Identify the parasite.
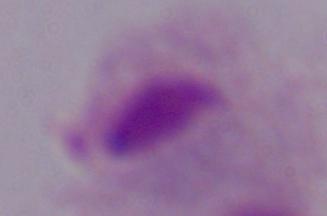
A trichomonad.

Summary:
  - Magnification: 1000x
  - Modality: photomicrograph